Classify this cell by malaria status.
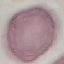
Uninfected.

preparation = thin blood smear
capture = smartphone through the microscope eyepiece
image type = cell patch, automatically extracted from a larger field of view and resized to 64 × 64 pixels
stain = Giemsa